State which parasite is depicted.
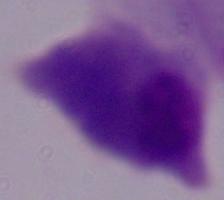
A trichomonad.

Summary:
  - Modality: micrograph
  - Magnification: 1000x